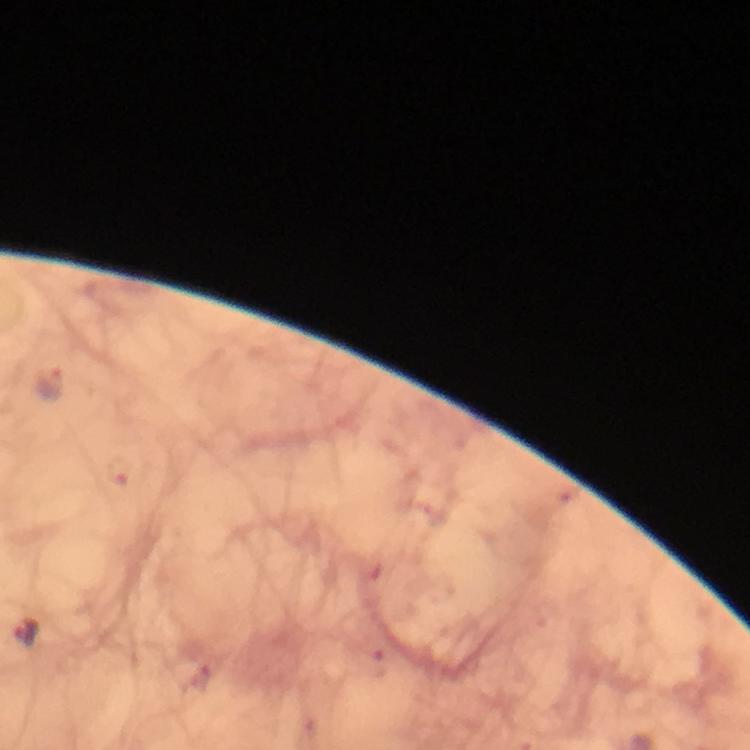

context = from a malaria diagnostic workup
preparation = thick blood film
cropped from = one field of view
magnification = 100x
image size = 750×750 pixels
malaria parasite locations = approximate centers as {x, y} in pixels: {49, 386}, {26, 631}
stain = Giemsa
immersion oil = applied
capture = smartphone mounted on the microscope